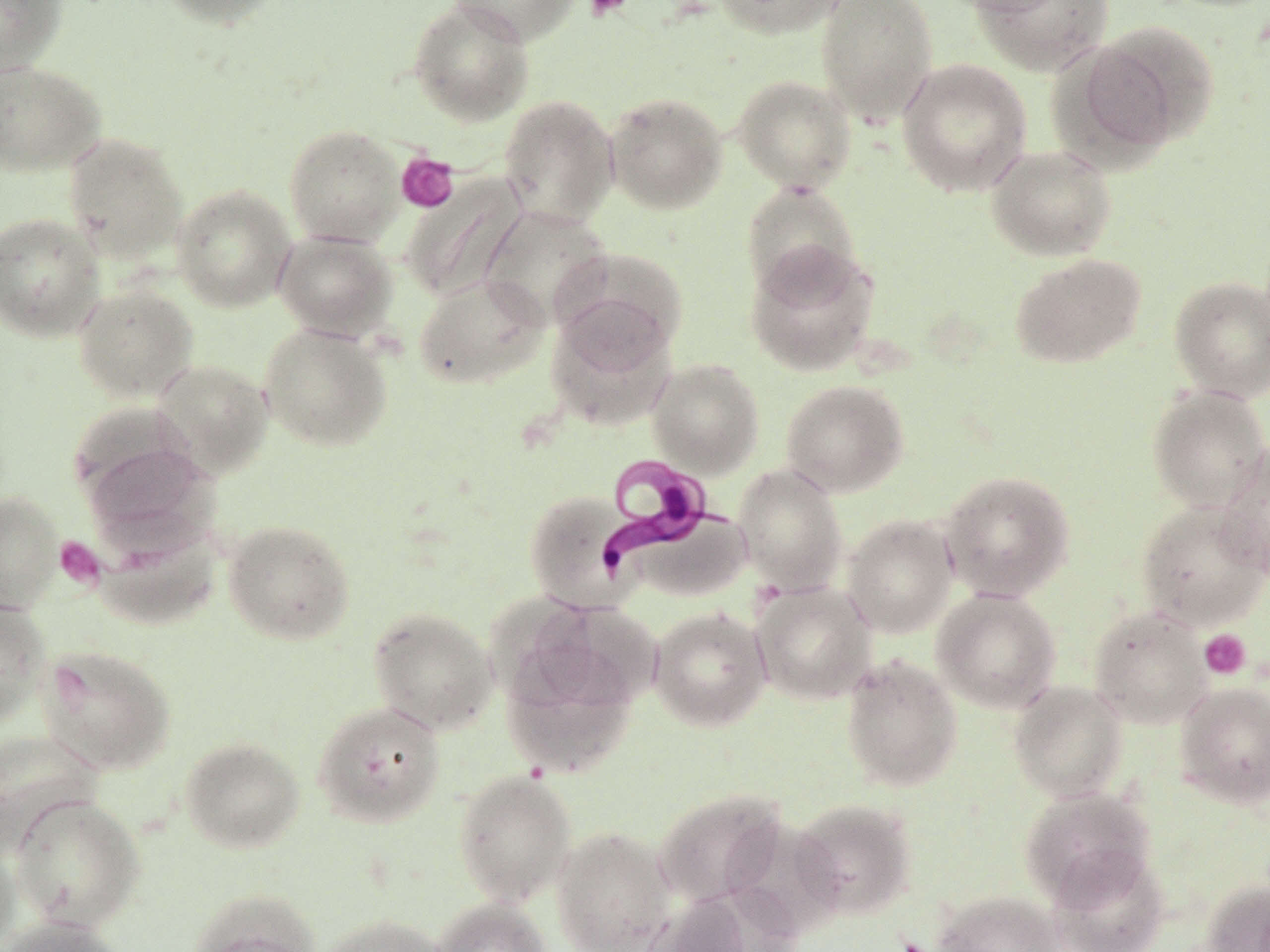
Summary:
  - Coordinate format: approximate bounding boxes as named x1/y1/x2/y2 corners in pixels
  - Trypanosoma brucei locations (subset): (x1=600, y1=453, x2=718, y2=576)
  - Uninfected red blood cell locations (subset): (x1=0, y1=0, x2=66, y2=75), (x1=157, y1=0, x2=284, y2=29), (x1=408, y1=0, x2=535, y2=126), (x1=447, y1=0, x2=579, y2=45), (x1=713, y1=0, x2=845, y2=38), (x1=815, y1=0, x2=938, y2=124), (x1=946, y1=0, x2=1067, y2=17), (x1=973, y1=0, x2=1113, y2=75), (x1=1078, y1=21, x2=1219, y2=154), (x1=896, y1=58, x2=1032, y2=196), (x1=0, y1=60, x2=107, y2=176), (x1=732, y1=74, x2=856, y2=193), (x1=604, y1=91, x2=728, y2=214), (x1=498, y1=94, x2=619, y2=227), (x1=284, y1=124, x2=405, y2=246), (x1=63, y1=133, x2=188, y2=263), (x1=985, y1=143, x2=1117, y2=260), (x1=401, y1=173, x2=528, y2=303), (x1=741, y1=181, x2=862, y2=300), (x1=171, y1=184, x2=297, y2=312), (x1=480, y1=206, x2=612, y2=327), (x1=0, y1=212, x2=106, y2=342), (x1=274, y1=228, x2=397, y2=341), (x1=744, y1=241, x2=881, y2=376), (x1=552, y1=246, x2=688, y2=369), (x1=1009, y1=253, x2=1147, y2=368), (x1=414, y1=272, x2=549, y2=389), (x1=1169, y1=275, x2=1270, y2=402), (x1=72, y1=283, x2=199, y2=403), (x1=545, y1=308, x2=678, y2=432), (x1=258, y1=322, x2=393, y2=451), (x1=150, y1=358, x2=274, y2=478), (x1=647, y1=358, x2=765, y2=477), (x1=780, y1=378, x2=910, y2=497), (x1=1147, y1=386, x2=1270, y2=513), (x1=81, y1=437, x2=218, y2=551), (x1=1217, y1=441, x2=1270, y2=579), (x1=734, y1=463, x2=848, y2=595), (x1=939, y1=469, x2=1076, y2=601), (x1=0, y1=490, x2=64, y2=612), (x1=1135, y1=499, x2=1270, y2=631), (x1=630, y1=506, x2=750, y2=603), (x1=842, y1=514, x2=957, y2=637), (x1=222, y1=518, x2=355, y2=645), (x1=90, y1=519, x2=223, y2=630), (x1=751, y1=581, x2=877, y2=705), (x1=930, y1=588, x2=1062, y2=714), (x1=0, y1=599, x2=51, y2=727), (x1=520, y1=599, x2=662, y2=716), (x1=368, y1=606, x2=498, y2=734), (x1=648, y1=606, x2=771, y2=731), (x1=1087, y1=606, x2=1212, y2=729), (x1=501, y1=634, x2=641, y2=778), (x1=37, y1=644, x2=176, y2=776), (x1=840, y1=654, x2=963, y2=791), (x1=1008, y1=681, x2=1128, y2=802), (x1=1174, y1=681, x2=1270, y2=808), (x1=312, y1=700, x2=446, y2=828), (x1=0, y1=728, x2=104, y2=854), (x1=179, y1=735, x2=305, y2=853), (x1=453, y1=769, x2=577, y2=907), (x1=1018, y1=786, x2=1156, y2=906), (x1=652, y1=788, x2=787, y2=908), (x1=9, y1=793, x2=145, y2=932), (x1=791, y1=798, x2=917, y2=919), (x1=551, y1=826, x2=676, y2=952), (x1=0, y1=838, x2=20, y2=952), (x1=1048, y1=847, x2=1171, y2=952), (x1=1199, y1=879, x2=1270, y2=952), (x1=188, y1=888, x2=321, y2=952), (x1=933, y1=890, x2=1064, y2=952), (x1=643, y1=893, x2=757, y2=952), (x1=430, y1=897, x2=553, y2=952), (x1=317, y1=914, x2=448, y2=952), (x1=0, y1=916, x2=128, y2=952)
  - Platelet locations: (x1=584, y1=0, x2=631, y2=20), (x1=396, y1=152, x2=459, y2=213), (x1=55, y1=537, x2=104, y2=589), (x1=1198, y1=629, x2=1252, y2=679)
  - Slide-level diagnosis: Trypanosoma brucei
  - Field of view: one of a larger specimen
  - Magnification: 1000x
  - Modality: optical microscopy
  - Preparation: thin blood film
  - Image size: 1270×952 pixels
  - Stain: May-Grünwald-Giemsa